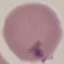
Malaria status: uninfected. Thin blood film. Photographed with a smartphone camera at the microscope eyepiece. Giemsa-stained preparation. Automatically extracted cell patch, resized to 64 × 64 pixels.